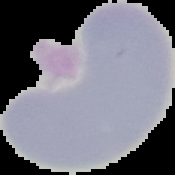

Summary:
  - Result: no malaria parasites detected
  - Image size: 175×175 pixels
  - Preparation: thin blood smear
  - Image type: cell region segmented out of the field of view; surrounding area masked to black